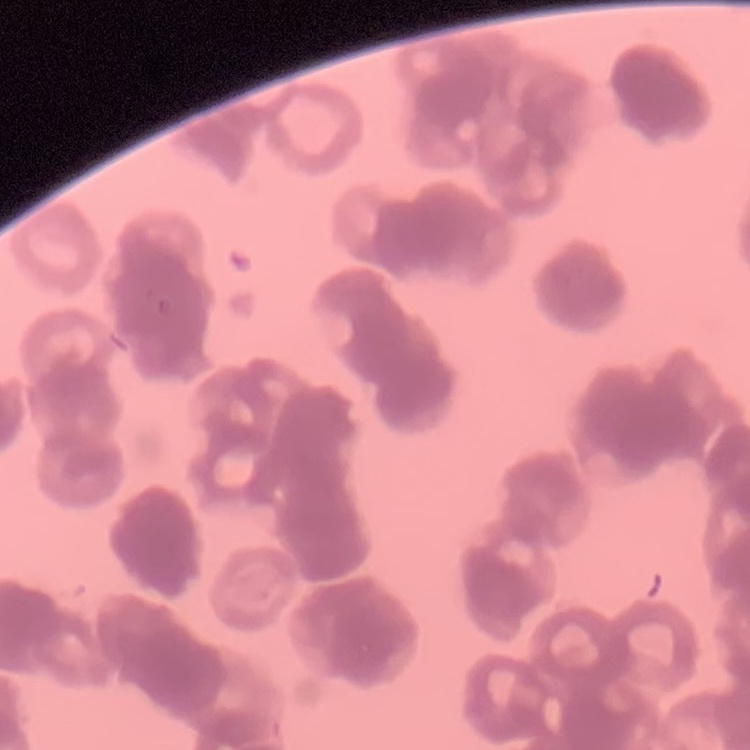
erythrocyte_morphology: rouleaux formation
preparation: thin blood smear
image_type: one tile cut from a larger photomicrograph
stain: Field's or Giemsa